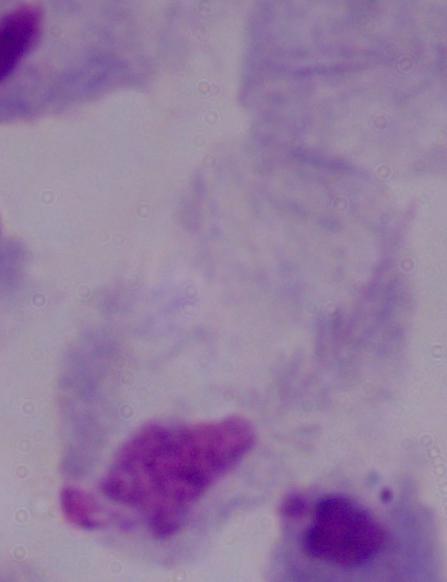

Summary:
  - Magnification: 1000x
  - Modality: photomicrograph
  - Identification: trichomonad